Draw a bounding box around every Plasmodium parasite.
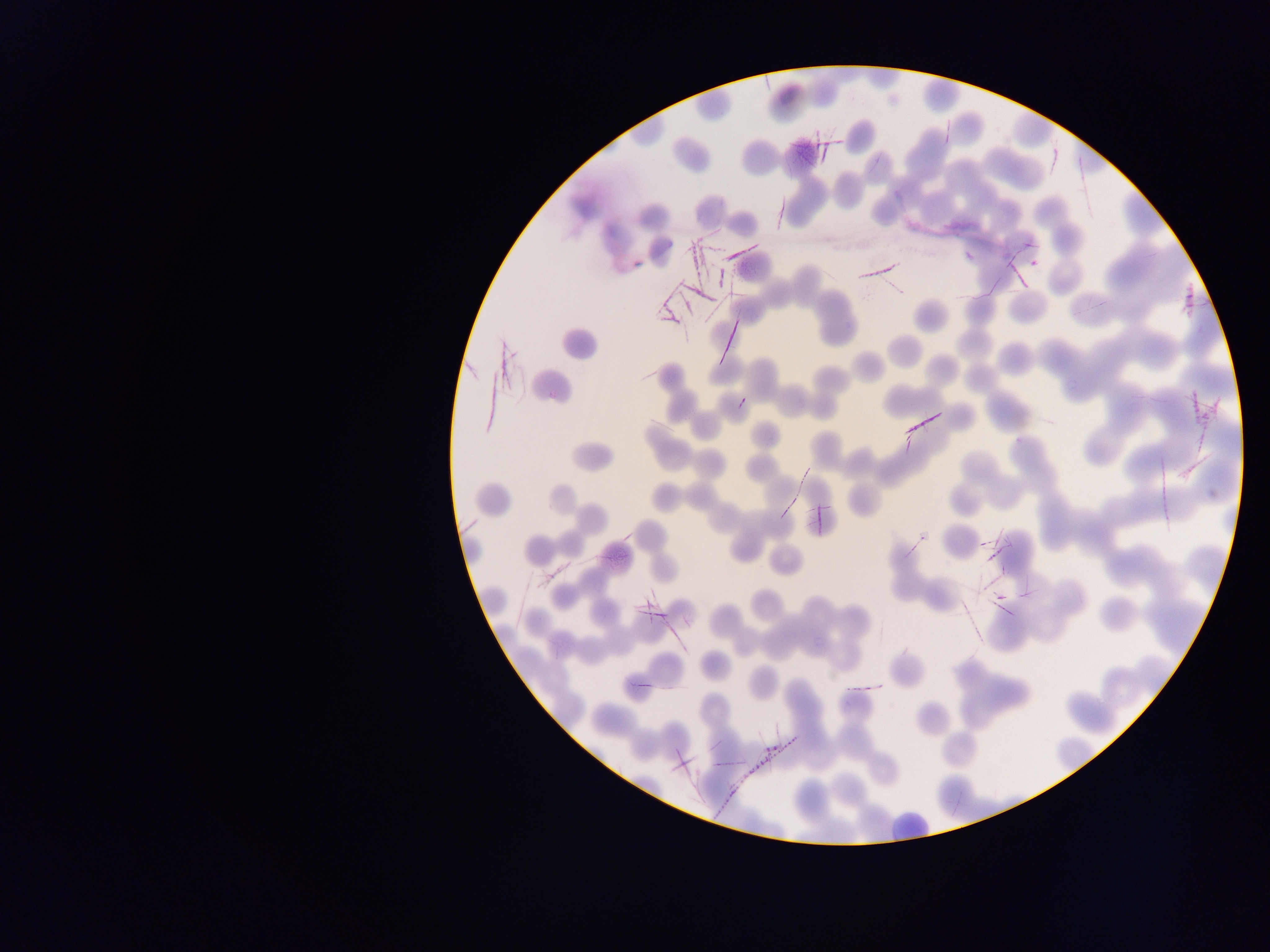
No Plasmodium parasites observed.

Approximate bounding boxes as {left, top, right, bottom} in pixels.
Summary:
  - Leukocyte locations: {881, 812, 937, 843}
  - Artifact (stain precipitate or debris) locations: {788, 133, 846, 166}, {684, 221, 744, 292}, {859, 251, 913, 278}, {1177, 268, 1201, 317}, {654, 286, 695, 328}, {709, 309, 742, 370}, {1189, 383, 1218, 430}, {902, 403, 945, 439}, {806, 498, 842, 526}, {958, 526, 1008, 635}, {639, 577, 682, 636}, {712, 727, 792, 817}, {668, 741, 702, 774}
  - Country: Ghana
  - Image size: 1270×952 pixels
  - Capture: mobile-phone photograph through a microscope
  - Field of view: single
  - Preparation: thin blood film